State which parasite is depicted.
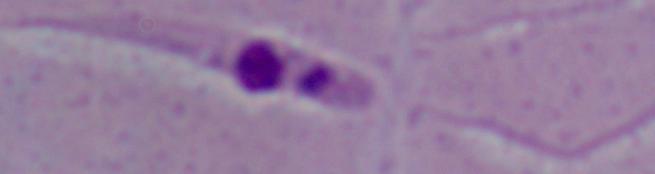
This is Leishmania.

Captured at 1000x magnification. Micrograph.